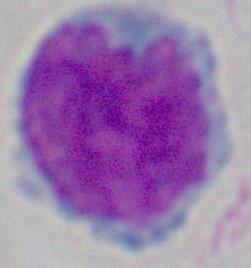

Summary:
  - Identification: leukocyte
  - Modality: micrograph
  - Magnification: 1000x